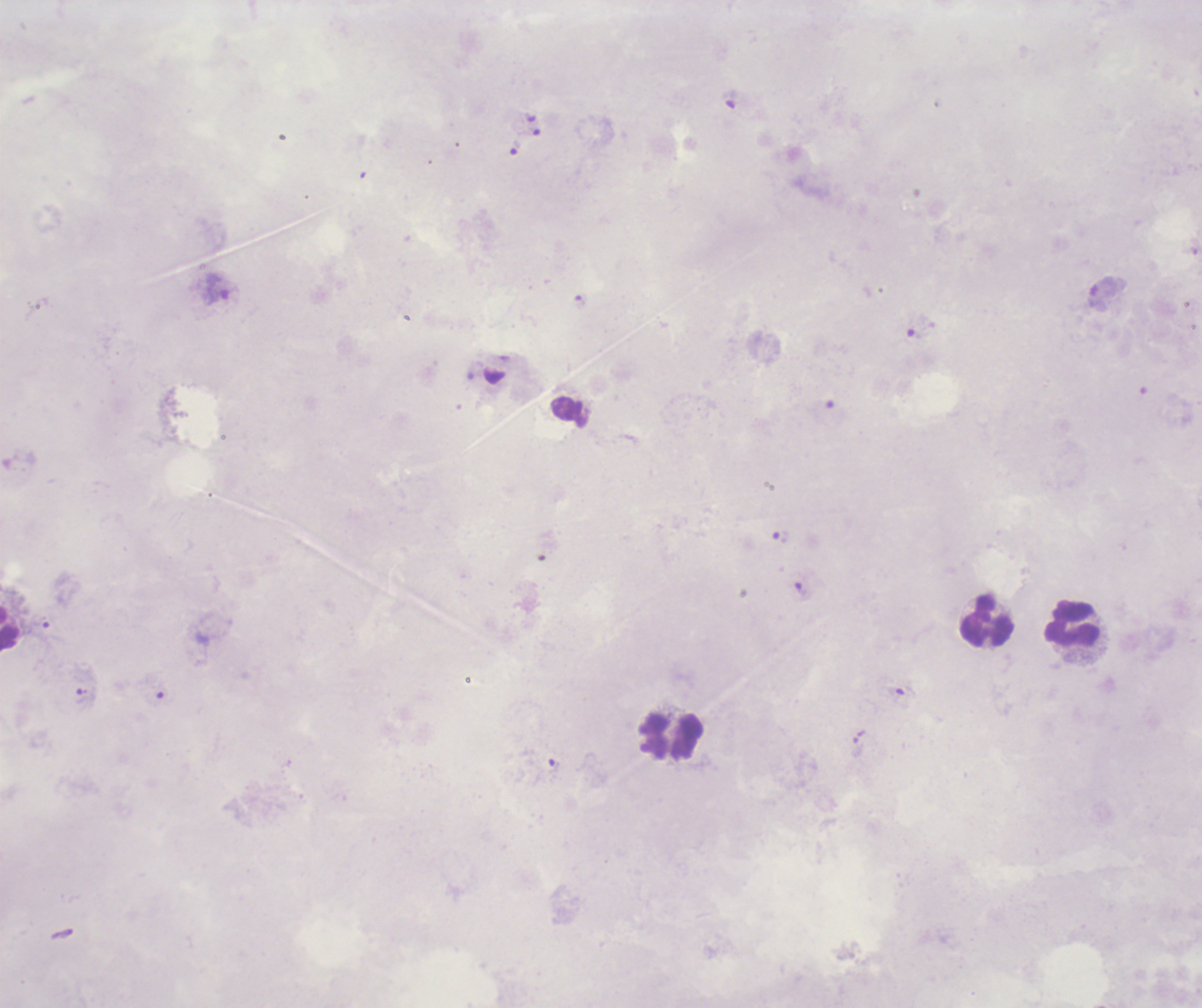
coordinate format = approximate object centers, in pixels from the top-left corner
trophozoite locations = (x=731, y=99), (x=217, y=288), (x=1106, y=288), (x=780, y=537), (x=800, y=589), (x=40, y=622), (x=904, y=689), (x=86, y=697), (x=858, y=736), (x=553, y=766)
leukocyte locations = (x=986, y=621), (x=1073, y=624), (x=9, y=629), (x=674, y=736)
field of view = single
result = Plasmodium parasites identified
preparation = thick smear of blood
image size = 1202×1008 pixels
magnification = 100x
background quality = poor
stain = Romanowsky
context = previously used in a real diagnosis
coloration quality = bad